Outline each blood parasite and name the species.
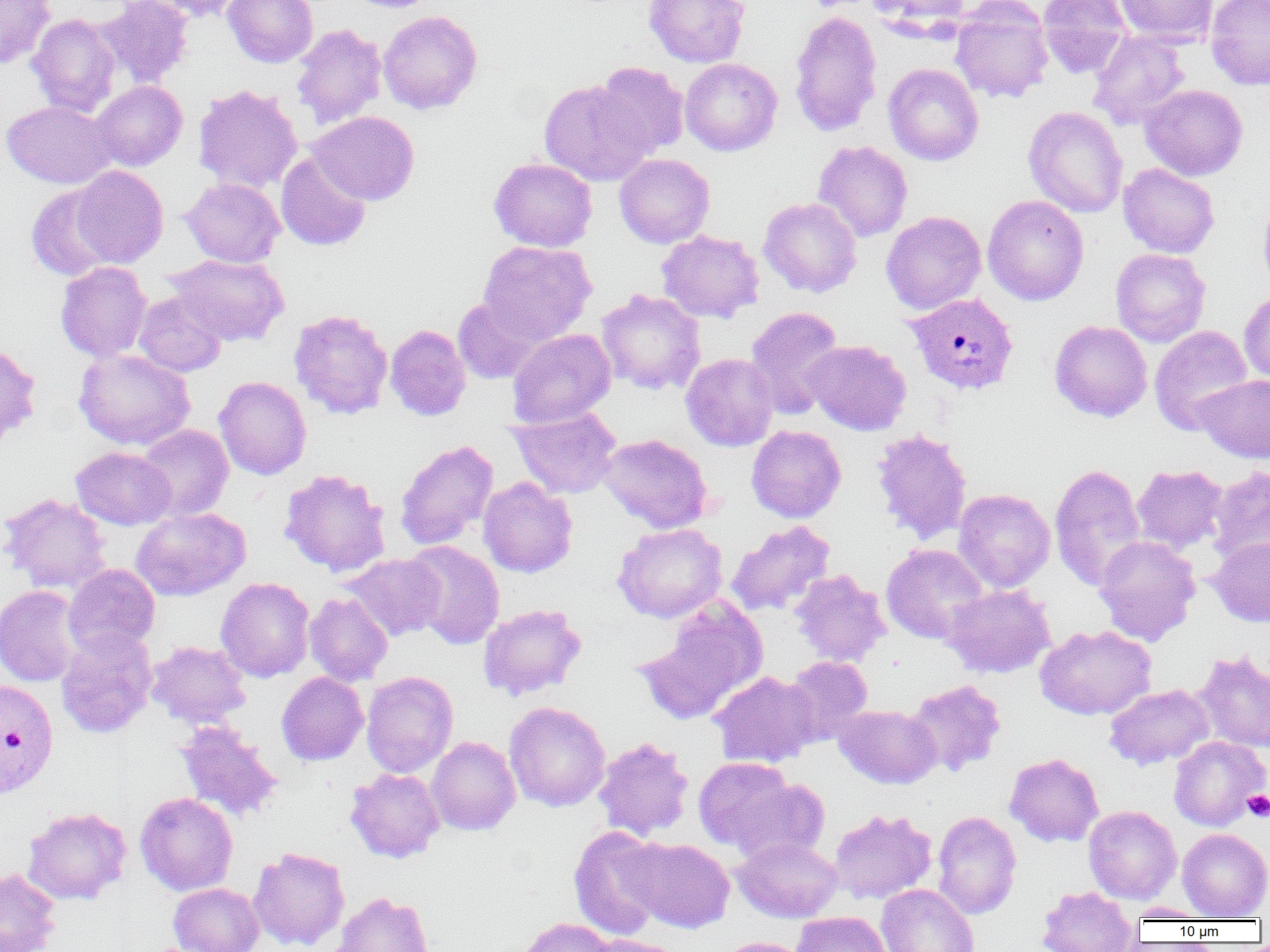
Approximate bounding boxes as (x1, y1, x2, y2) in pixels.
Plasmodium vivax-infected red blood cells: (904, 292, 1019, 396), (0, 679, 59, 798).
No Plasmodium falciparum, Plasmodium ovale, Plasmodium malariae, Babesia divergens, or Trypanosoma brucei observed.

slide-level diagnosis = Plasmodium vivax
platelet locations = approximate bounding boxes as (x1, y1, x2, y2) in pixels: (1242, 789, 1270, 821)
uninfected red blood cell locations = approximate bounding boxes as (x1, y1, x2, y2) in pixels: (96, 0, 194, 88), (137, 0, 250, 22), (223, 0, 319, 68), (344, 0, 443, 13), (644, 0, 750, 68), (867, 0, 970, 34), (1037, 0, 1133, 78), (1114, 0, 1218, 46), (1205, 0, 1270, 91), (0, 1, 55, 68), (950, 1, 1054, 103), (789, 9, 883, 137), (378, 10, 483, 114), (26, 14, 122, 116), (291, 23, 387, 129), (1088, 31, 1189, 130), (680, 57, 782, 156), (605, 61, 698, 248), (594, 62, 689, 159), (883, 63, 984, 165), (539, 79, 654, 186), (90, 81, 187, 171), (193, 84, 303, 194), (1140, 84, 1248, 180), (2, 101, 117, 188), (1023, 106, 1128, 218), (308, 111, 420, 206), (813, 141, 913, 242), (275, 152, 371, 251), (614, 153, 715, 248), (489, 157, 598, 252), (1118, 163, 1220, 258), (69, 165, 169, 268), (180, 178, 284, 268), (27, 184, 118, 281), (982, 194, 1089, 305), (758, 197, 862, 298), (1257, 197, 1270, 296), (881, 211, 986, 315), (656, 230, 764, 324), (477, 240, 597, 344), (1110, 248, 1211, 347), (166, 254, 289, 346), (55, 261, 152, 362), (597, 289, 706, 395), (133, 291, 228, 377), (1239, 291, 1270, 385), (452, 295, 549, 385), (745, 307, 844, 419), (288, 309, 393, 419), (1049, 320, 1152, 421), (385, 324, 471, 422), (1149, 325, 1253, 435), (507, 328, 616, 428), (803, 340, 912, 435), (0, 342, 42, 444), (73, 348, 195, 450), (681, 353, 778, 451), (1194, 374, 1270, 463), (214, 376, 311, 480), (508, 406, 623, 499), (135, 424, 234, 521), (746, 425, 846, 523), (871, 428, 973, 544), (597, 433, 713, 533), (394, 439, 498, 550), (70, 446, 176, 530), (1049, 463, 1146, 591), (1132, 464, 1228, 554), (1207, 465, 1270, 565), (278, 468, 391, 577), (478, 477, 577, 578), (953, 488, 1055, 592), (0, 493, 112, 595), (131, 507, 251, 601), (726, 520, 835, 616), (612, 523, 728, 623), (1094, 535, 1201, 645), (1208, 537, 1270, 627), (403, 540, 505, 650), (881, 544, 989, 644), (342, 553, 446, 641), (63, 564, 160, 658), (790, 569, 891, 667), (215, 577, 315, 681), (0, 584, 84, 687), (942, 584, 1056, 678), (304, 593, 393, 686), (636, 600, 768, 724), (478, 603, 587, 701), (1035, 625, 1156, 720), (56, 629, 157, 738), (146, 641, 251, 728), (1193, 651, 1270, 754), (783, 655, 873, 745), (361, 670, 459, 777), (709, 671, 820, 768), (276, 672, 368, 766), (905, 679, 1006, 777), (1104, 684, 1213, 769), (504, 701, 610, 812), (834, 704, 941, 789), (174, 720, 283, 822), (425, 736, 521, 836), (593, 736, 694, 841), (1169, 736, 1269, 831), (1005, 753, 1104, 847), (693, 756, 800, 854), (345, 768, 446, 863), (726, 774, 832, 864), (135, 792, 238, 896), (22, 806, 131, 905), (1083, 806, 1181, 903), (829, 808, 937, 904), (932, 811, 1021, 920), (569, 826, 669, 940), (1177, 828, 1270, 920), (626, 837, 735, 933), (733, 838, 842, 922), (247, 846, 350, 951), (0, 868, 61, 952), (169, 883, 264, 952), (876, 883, 979, 952), (1037, 886, 1138, 952), (331, 891, 436, 952), (1125, 903, 1212, 921), (791, 911, 891, 952), (514, 917, 616, 952), (579, 934, 686, 952), (714, 936, 812, 952)
image size = 1270×952 pixels
modality = light microscopy
field of view = single
preparation = thin blood smear
magnification = 1000x